Outline each blood parasite and name the species.
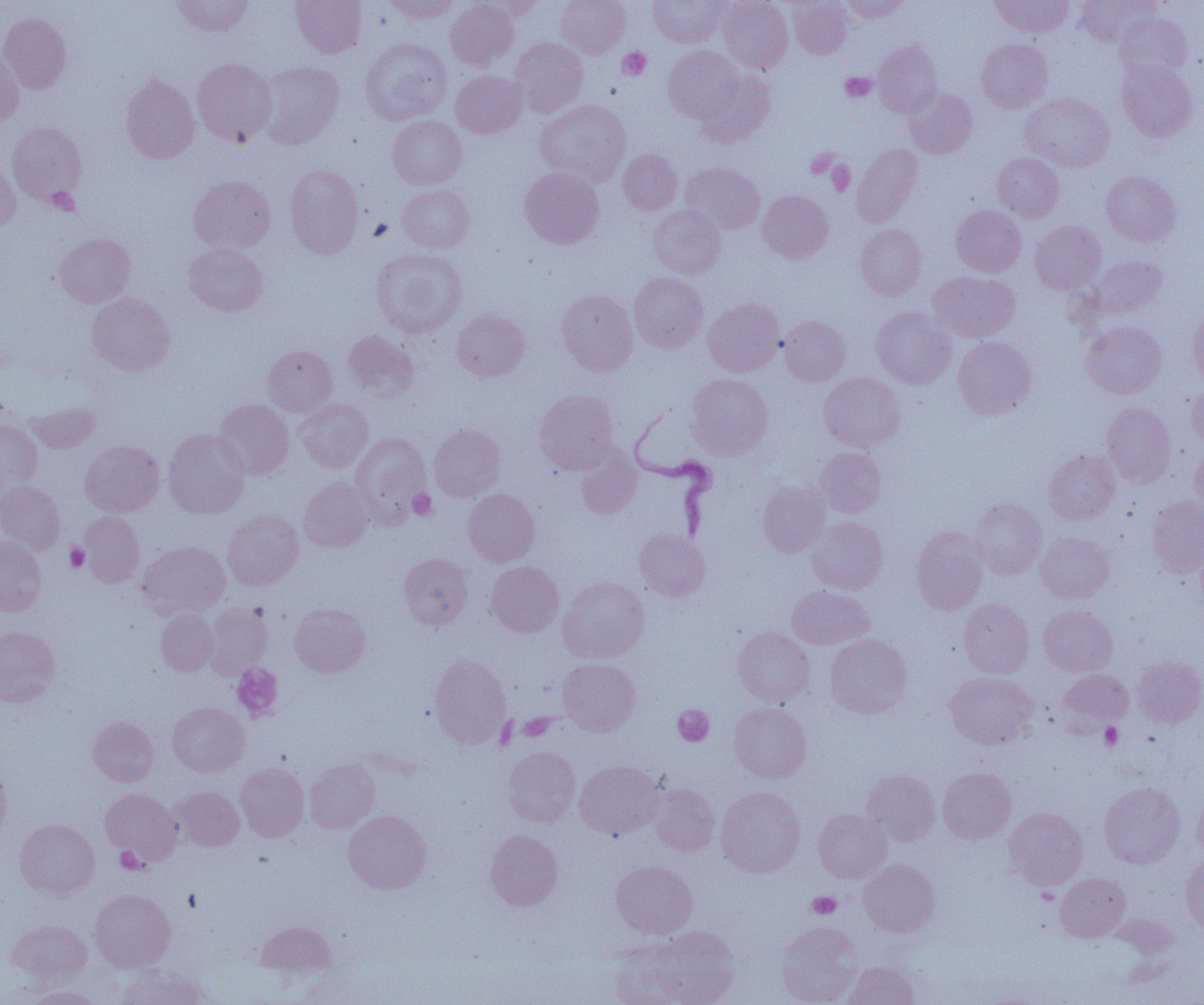

Approximate bounding boxes as (x1, y1, x2, y2) in pixels.
Trypanosoma brucei: (629, 409, 718, 543).
No Plasmodium falciparum, Plasmodium ovale, Plasmodium malariae, Plasmodium vivax, or Babesia divergens observed.

Summary:
  - Platelet locations: (617, 48, 651, 80), (840, 73, 876, 102), (806, 149, 839, 179), (827, 161, 855, 195), (46, 187, 78, 215), (408, 489, 437, 520), (65, 543, 88, 571), (231, 663, 283, 721), (672, 705, 714, 746), (518, 713, 555, 741), (1100, 723, 1122, 750), (115, 847, 143, 873), (1037, 888, 1058, 905), (807, 891, 841, 919)
  - Uninfected red blood cell locations: (171, 0, 254, 36), (291, 0, 367, 58), (382, 0, 460, 23), (446, 0, 518, 70), (472, 0, 542, 21), (556, 0, 630, 58), (648, 0, 729, 48), (718, 0, 793, 74), (787, 0, 853, 59), (842, 0, 911, 22), (990, 0, 1074, 38), (1077, 0, 1160, 46), (1114, 12, 1192, 80), (0, 13, 71, 93), (360, 38, 451, 124), (511, 38, 588, 117), (977, 38, 1053, 112), (873, 41, 942, 117), (663, 45, 744, 123), (0, 48, 24, 126), (192, 58, 276, 146), (1117, 59, 1198, 141), (257, 62, 344, 148), (451, 70, 527, 138), (695, 70, 776, 146), (120, 73, 199, 163), (904, 88, 977, 158), (1021, 93, 1114, 172), (535, 99, 631, 187), (387, 115, 467, 189), (6, 121, 87, 205), (852, 143, 923, 227), (617, 149, 682, 215), (992, 153, 1064, 222), (0, 159, 20, 234), (680, 163, 765, 234), (284, 165, 364, 258), (520, 167, 604, 249), (1101, 171, 1181, 245), (189, 176, 275, 254), (397, 185, 474, 253), (757, 190, 833, 263), (649, 205, 725, 279), (951, 205, 1026, 276), (1030, 220, 1106, 294), (855, 224, 926, 300), (55, 233, 135, 307), (184, 243, 269, 316), (372, 248, 466, 337), (1082, 256, 1167, 322), (928, 271, 1020, 342), (629, 272, 708, 353), (556, 291, 638, 375), (87, 293, 175, 376), (703, 299, 784, 376), (870, 306, 956, 388), (1188, 306, 1204, 387), (452, 308, 530, 381), (780, 317, 850, 385), (1081, 321, 1166, 398), (342, 331, 419, 402), (953, 336, 1036, 419), (263, 345, 337, 416), (685, 373, 773, 458), (819, 373, 905, 451), (1185, 385, 1204, 446), (535, 390, 618, 473), (214, 399, 294, 480), (295, 399, 373, 472), (26, 402, 100, 454), (1102, 402, 1176, 487), (0, 420, 42, 495), (429, 425, 505, 501), (163, 429, 250, 518), (351, 433, 431, 521), (80, 440, 164, 517), (1191, 446, 1204, 514), (575, 447, 641, 518), (814, 447, 886, 517), (1044, 450, 1120, 524), (299, 477, 374, 552), (0, 481, 65, 554), (757, 481, 830, 556), (463, 488, 540, 566), (1146, 495, 1204, 577), (969, 499, 1047, 579), (223, 510, 303, 590), (79, 511, 144, 588), (807, 516, 888, 594), (911, 526, 989, 614), (634, 529, 710, 601), (1036, 532, 1114, 603), (0, 535, 47, 617), (136, 541, 230, 620), (398, 553, 472, 630), (486, 562, 564, 637), (558, 576, 649, 664), (787, 586, 874, 649), (959, 599, 1034, 678), (203, 604, 272, 678), (290, 604, 371, 677), (1038, 605, 1117, 676), (156, 609, 217, 675), (0, 626, 60, 706), (733, 627, 815, 707), (825, 634, 913, 718), (1132, 654, 1204, 728), (429, 655, 511, 747), (558, 659, 641, 735), (1058, 669, 1133, 731), (945, 672, 1037, 749), (168, 702, 249, 776), (729, 703, 811, 783), (88, 715, 158, 786), (502, 747, 580, 826), (305, 759, 379, 833), (574, 760, 662, 839), (0, 763, 11, 840), (236, 763, 309, 841), (938, 768, 1016, 844), (862, 770, 941, 845), (1099, 782, 1184, 868), (649, 783, 720, 856), (171, 786, 244, 851), (716, 786, 805, 877), (100, 788, 181, 864), (1194, 793, 1204, 864), (1004, 807, 1088, 889), (813, 809, 892, 883), (343, 810, 431, 894), (15, 819, 99, 899), (485, 829, 563, 910), (1181, 856, 1204, 934), (859, 859, 940, 937), (611, 860, 697, 938), (1055, 873, 1130, 942), (90, 889, 175, 972), (7, 920, 91, 986), (256, 921, 336, 979), (776, 921, 862, 1005), (620, 926, 739, 1005), (843, 961, 919, 1005), (116, 965, 212, 1005), (25, 986, 103, 1004)
  - Slide-level diagnosis: Trypanosoma brucei
  - Field of view: single
  - Magnification: 1000x
  - Preparation: thin blood film
  - Image size: 1204×1005 pixels
  - Modality: optical microscopy